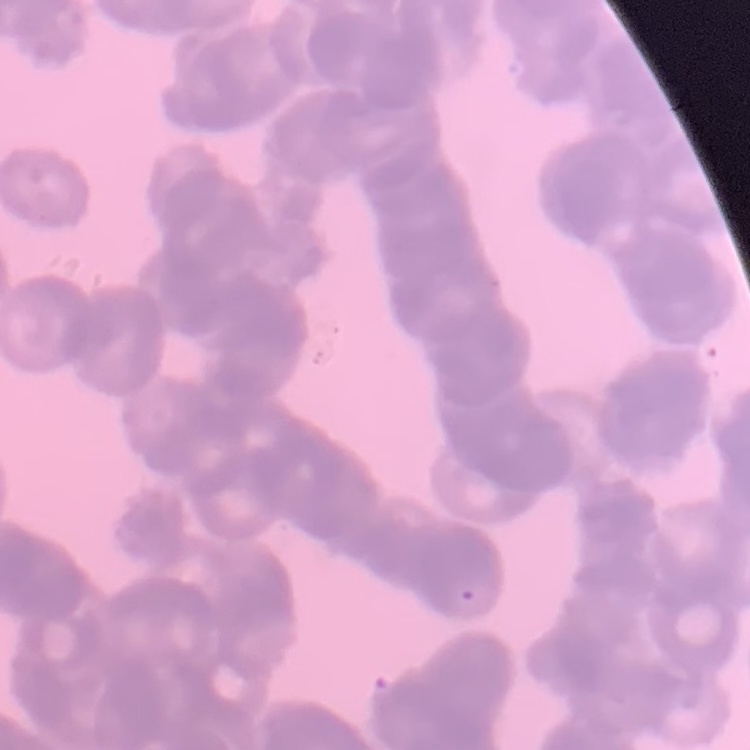

The red blood cells show rouleaux formation. Thin peripheral smear. Square crop of a larger photomicrograph. Field's or Giemsa stain.